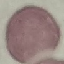
malaria status = uninfected
preparation = thin smear
image type = cell patch, automatically extracted from a larger field of view and resized to 64 × 64 pixels
stain = Giemsa
capture = smartphone camera at the microscope eyepiece